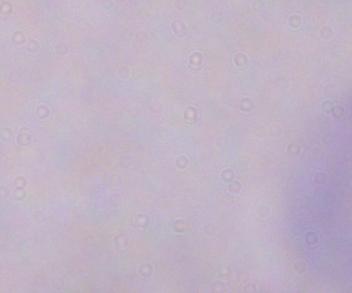 Micrograph. A trypanosome is shown. Captured at 1000x magnification.